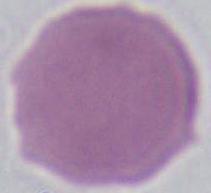
Captured at 1000x magnification. Photomicrograph. An erythrocyte is shown.